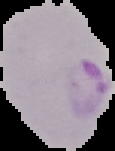

Summary:
  - Image type: cell region segmented out of the field of view; surrounding area masked to black
  - Malaria status: parasitized
  - Preparation: thin blood smear
  - Image size: 115×151 pixels